Assess this cell for malaria.
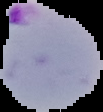

Parasitized.

From a thin blood smear. Image is 103×112 pixels. The area outside the segmented cell region is set to black.